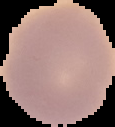

image type = cell region segmented out of the field of view; surrounding area masked to black
malaria status = uninfected
preparation = thin blood smear
image size = 115×127 pixels